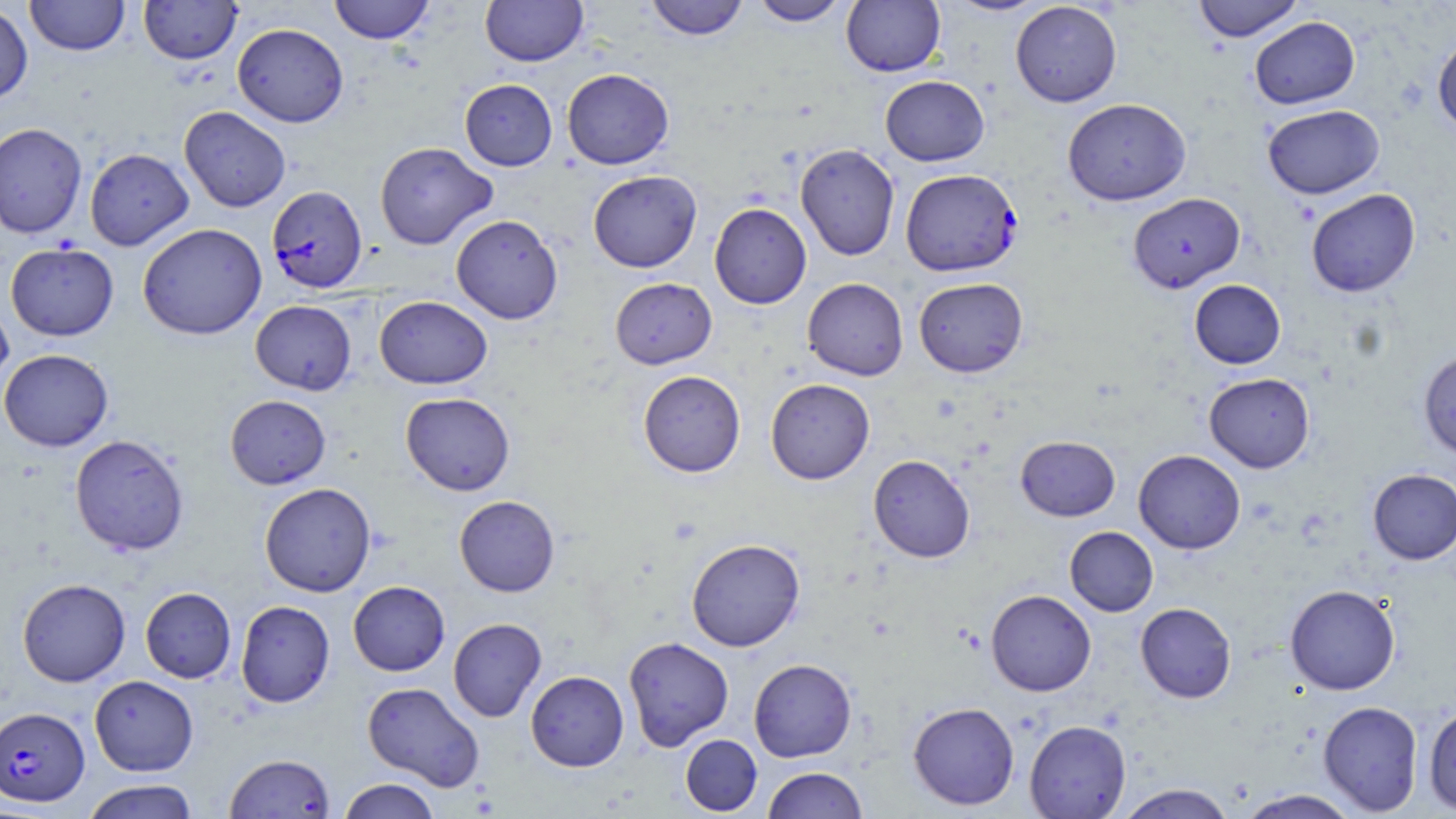
Approximate bounding boxes as [x1, y1, x2, y2] in pixels. Plasmodium falciparum-infected red blood cell locations: [900, 175, 1027, 271], [266, 185, 368, 294], [0, 707, 89, 807]. Uninfected red blood cell locations: [25, 0, 129, 56], [139, 0, 241, 64], [328, 0, 435, 44], [481, 0, 588, 67], [644, 0, 749, 41], [750, 0, 850, 26], [841, 0, 945, 76], [941, 0, 1053, 17], [1192, 0, 1304, 42], [1010, 1, 1122, 107], [0, 3, 33, 105], [1249, 16, 1360, 109], [232, 23, 348, 127], [1433, 32, 1456, 138], [562, 68, 674, 169], [880, 75, 989, 166], [460, 79, 557, 171], [1062, 98, 1191, 205], [1262, 104, 1384, 199], [179, 106, 291, 212], [0, 122, 87, 238], [375, 142, 497, 249], [795, 143, 900, 261], [84, 148, 194, 250], [588, 170, 702, 272], [1306, 189, 1420, 297], [1128, 192, 1245, 293], [709, 203, 811, 309], [451, 214, 563, 324], [137, 223, 267, 340], [5, 243, 119, 341], [610, 277, 717, 369], [914, 277, 1028, 377], [802, 278, 908, 380], [1189, 279, 1286, 369], [0, 295, 14, 393], [375, 296, 492, 389], [250, 300, 357, 395], [1418, 348, 1456, 460], [0, 349, 114, 451], [638, 370, 746, 477], [1204, 373, 1315, 473], [766, 378, 875, 484], [400, 392, 516, 495], [225, 395, 331, 489], [69, 434, 189, 556], [1015, 436, 1120, 521], [1134, 449, 1245, 553], [868, 454, 975, 562], [1368, 468, 1456, 564], [259, 482, 376, 597], [454, 495, 560, 596], [1065, 526, 1158, 616], [686, 538, 805, 651], [17, 578, 131, 687], [348, 581, 450, 676], [1285, 584, 1400, 694], [140, 587, 236, 683], [986, 589, 1096, 696], [235, 600, 335, 707], [1135, 602, 1236, 703], [448, 618, 546, 722], [623, 636, 734, 750], [748, 658, 857, 762], [525, 670, 629, 771], [89, 675, 198, 776], [362, 681, 485, 791], [908, 701, 1020, 810], [1318, 701, 1423, 816], [1423, 705, 1456, 813], [1024, 719, 1131, 818], [680, 734, 762, 815], [224, 753, 335, 818], [762, 766, 868, 818], [337, 778, 441, 819], [80, 779, 201, 819], [1114, 784, 1237, 819], [1235, 789, 1361, 819]. Slide-level diagnosis: Plasmodium falciparum. Image is 1456×819 pixels. Optical microscopy. One field of a larger specimen. Thin blood smear. May-Grünwald-Giemsa stain. Captured at 1000x magnification.